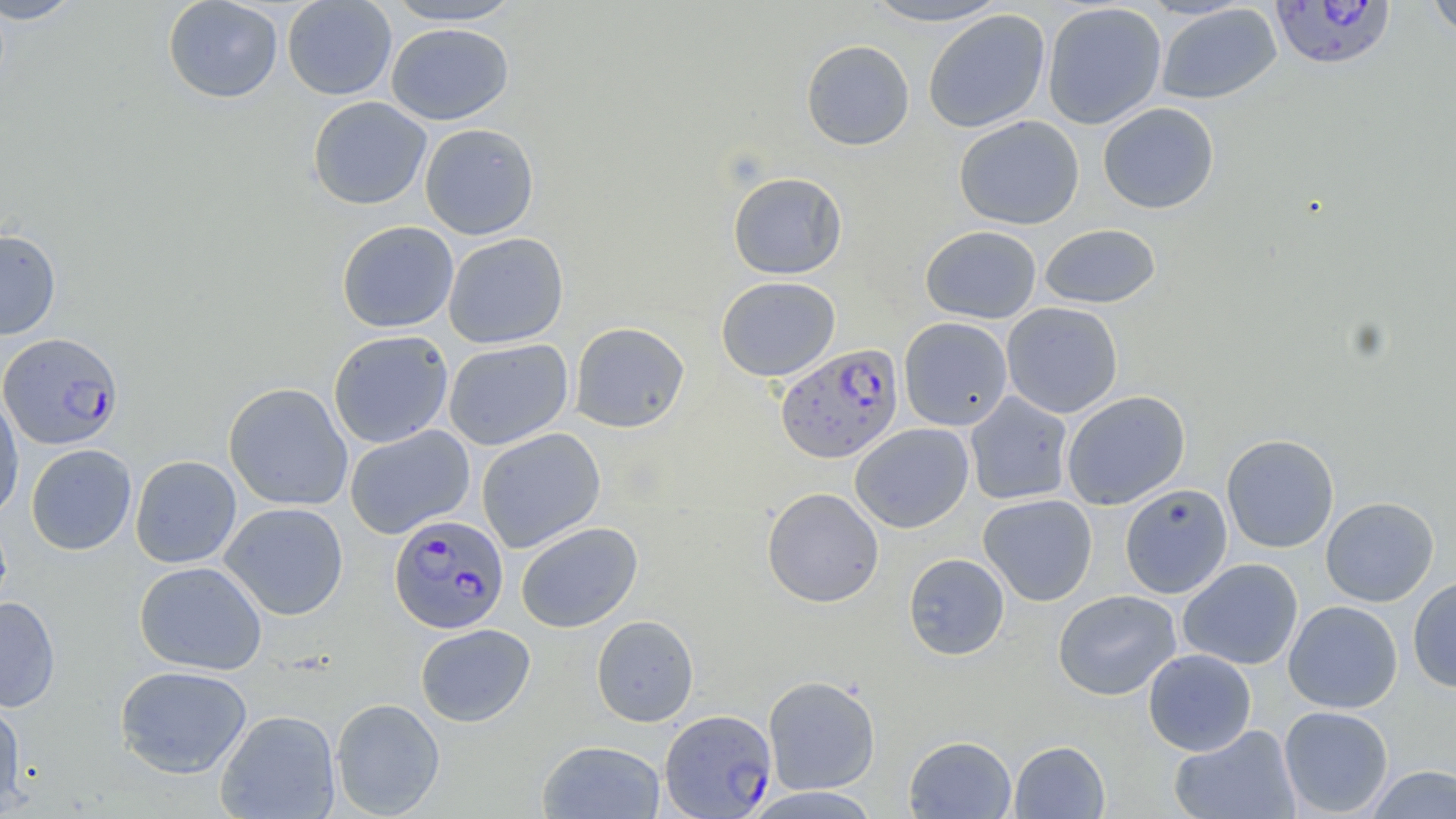

Approximate bounding boxes as [x1, y1, x2, y2] in pixels. Plasmodium falciparum-infected red blood cell locations: [1270, 1, 1397, 71], [0, 332, 124, 450], [775, 343, 903, 463], [389, 514, 509, 634], [659, 709, 777, 818]. Uninfected red blood cell locations: [0, 0, 85, 24], [162, 0, 284, 103], [282, 0, 396, 100], [383, 0, 528, 26], [860, 0, 1012, 28], [1425, 0, 1456, 40], [1042, 2, 1167, 130], [1156, 3, 1282, 104], [923, 10, 1051, 133], [386, 23, 514, 125], [801, 39, 915, 151], [307, 96, 431, 210], [1097, 102, 1220, 214], [953, 116, 1084, 229], [420, 122, 539, 240], [727, 171, 848, 279], [336, 220, 459, 333], [1039, 223, 1161, 308], [920, 225, 1042, 323], [0, 228, 61, 339], [443, 232, 569, 349], [716, 276, 841, 382], [1001, 302, 1123, 418], [898, 317, 1013, 430], [569, 321, 690, 433], [328, 330, 454, 448], [443, 338, 573, 450], [224, 382, 353, 511], [0, 391, 25, 522], [965, 391, 1074, 505], [1062, 391, 1190, 510], [850, 423, 974, 533], [344, 425, 475, 539], [477, 428, 606, 552], [1221, 434, 1339, 552], [25, 444, 137, 555], [130, 455, 241, 568], [1119, 484, 1233, 598], [762, 487, 884, 607], [978, 494, 1097, 606], [1320, 496, 1439, 606], [220, 502, 349, 620], [516, 521, 643, 633], [903, 553, 1010, 660], [1178, 558, 1303, 670], [134, 561, 268, 675], [1408, 576, 1456, 692], [1052, 589, 1182, 700], [0, 596, 61, 713], [1283, 601, 1402, 713], [591, 614, 699, 727], [415, 623, 535, 727], [1143, 649, 1257, 756], [114, 665, 253, 778], [763, 675, 881, 795], [330, 698, 445, 818], [0, 699, 27, 815], [1279, 706, 1393, 817], [215, 709, 340, 818], [1169, 724, 1302, 819], [904, 735, 1017, 818], [537, 740, 665, 819], [1009, 741, 1110, 818], [1365, 764, 1456, 818], [743, 786, 883, 818]. Slide-level diagnosis: Plasmodium falciparum. Thin blood smear. Captured at 1000x magnification. Optical microscopy. Image is 1456×819 pixels. May-Grünwald-Giemsa-stained preparation. Single field of view.